Give the extent of all uninfected red blood cells.
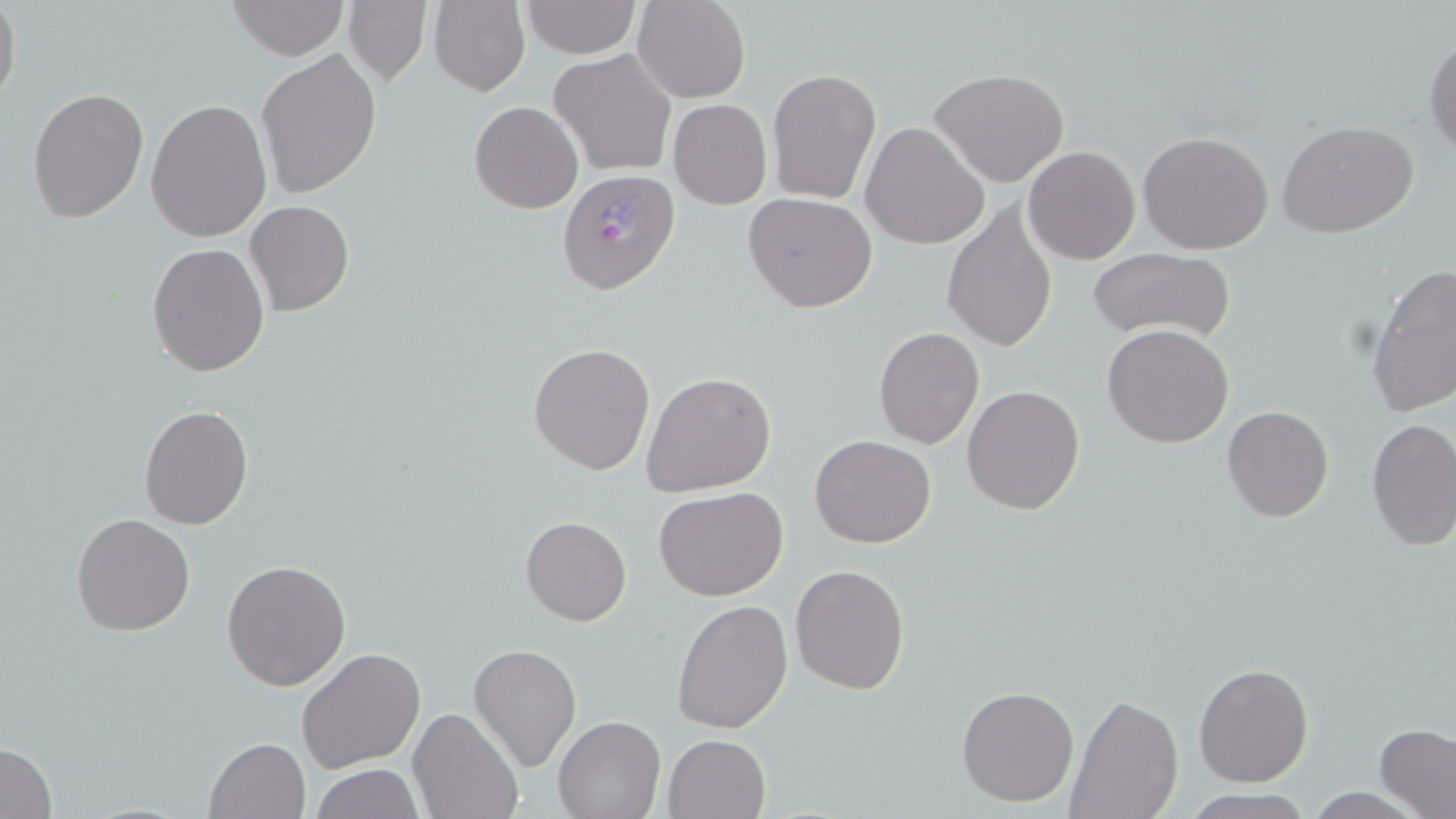

Approximate bounding boxes as (x1, y1, x2, y2) in pixels.
Uninfected red blood cells: (0, 0, 22, 112), (228, 0, 348, 59), (429, 0, 530, 97), (634, 0, 750, 104), (342, 1, 432, 87), (522, 1, 640, 57), (1423, 34, 1456, 157), (256, 49, 383, 197), (549, 49, 676, 177), (930, 68, 1070, 187), (767, 69, 882, 205), (26, 88, 148, 222), (145, 97, 272, 242), (668, 99, 772, 209), (470, 101, 583, 214), (1277, 120, 1421, 240), (860, 123, 988, 250), (1136, 131, 1275, 256), (1024, 146, 1141, 264), (743, 192, 877, 312), (245, 201, 353, 316), (942, 202, 1057, 353), (146, 244, 269, 376), (1087, 247, 1235, 344), (1365, 263, 1456, 419), (1102, 324, 1234, 449), (873, 326, 985, 449), (529, 342, 656, 475), (643, 372, 777, 498), (961, 385, 1085, 515), (137, 404, 254, 529), (1222, 405, 1333, 523), (1366, 419, 1456, 553), (810, 434, 937, 548), (654, 487, 788, 602), (71, 513, 195, 636), (521, 515, 632, 626), (222, 558, 351, 691), (789, 564, 911, 696), (671, 599, 793, 735), (467, 643, 581, 773), (296, 648, 424, 774), (1193, 663, 1313, 787), (956, 684, 1079, 807), (1065, 693, 1181, 817), (408, 706, 524, 819), (553, 715, 665, 819), (1375, 724, 1455, 818), (662, 734, 769, 819), (204, 737, 310, 819), (1, 741, 58, 818), (312, 764, 422, 819), (1180, 790, 1312, 819).

Plasmodium falciparum-infected red blood cell locations: (555, 169, 679, 294). Slide-level diagnosis: Plasmodium falciparum. May-Grünwald-Giemsa-stained preparation. Image is 1456×819 pixels. Single field of view. Thin blood smear. 1000x magnification. Optical microscopy.